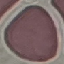

malaria status = uninfected
preparation = thin blood film
capture = smartphone camera at the microscope eyepiece
stain = Giemsa
image type = cell patch, automatically extracted from a larger field of view and resized to 64 × 64 pixels